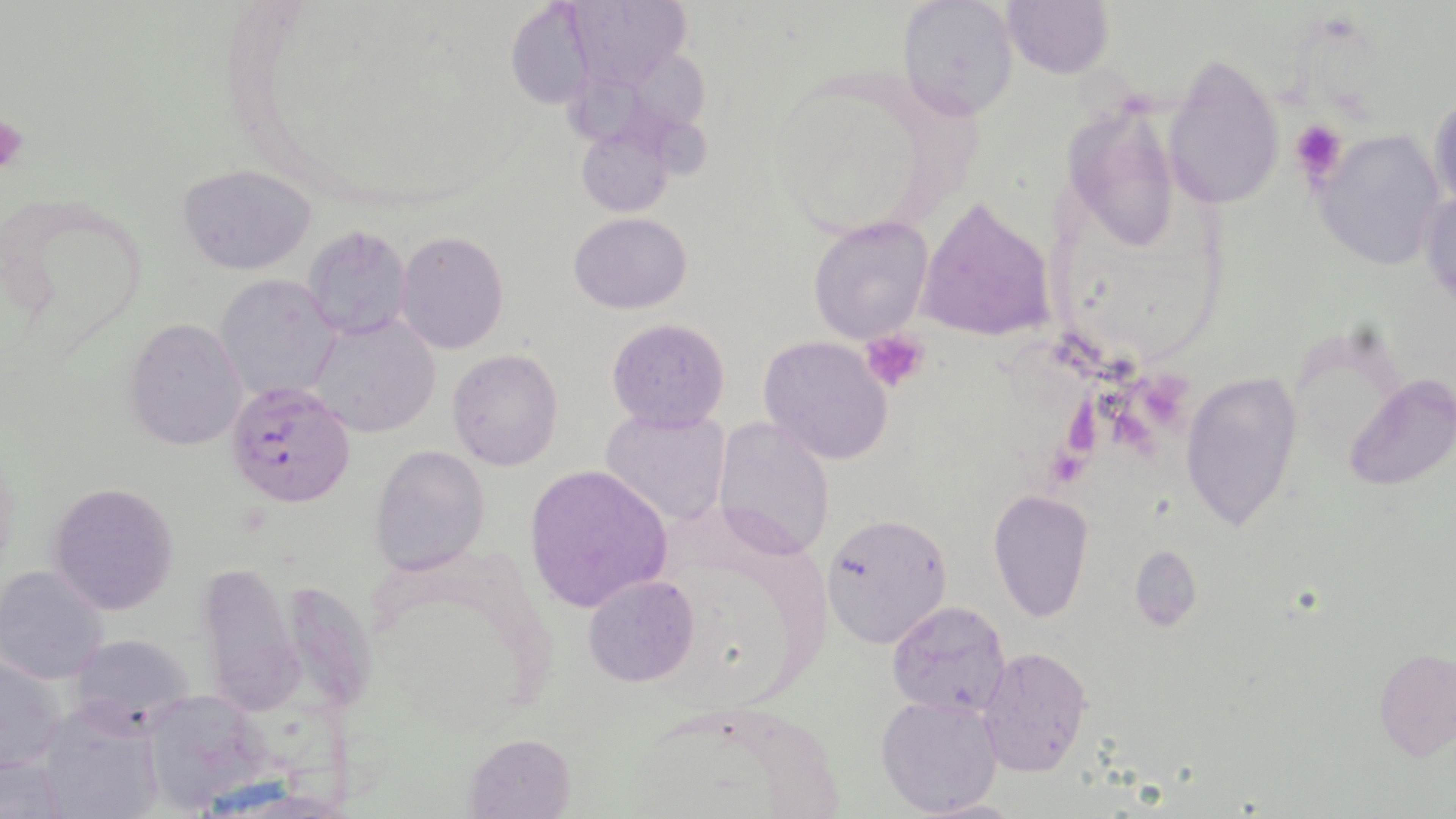

Summary:
  - Coordinate format: approximate bounding boxes as (x1,y1)-(x2,y2) corner pairs in pixels
  - Platelet locations: (0,112)-(28,177), (1289,117)-(1348,186), (860,330)-(932,394)
  - Uninfected red blood cell locations: (562,0)-(695,92), (1001,0)-(1115,78), (502,1)-(602,110), (896,1)-(1017,121), (1163,53)-(1284,211), (1429,89)-(1455,216), (1068,103)-(1178,259), (576,125)-(677,216), (1313,129)-(1446,270), (177,163)-(317,276), (1420,185)-(1455,311), (917,196)-(1058,344), (568,212)-(693,313), (806,215)-(933,345), (300,223)-(414,342), (395,232)-(509,354), (215,273)-(341,405), (310,315)-(441,438), (124,317)-(246,451), (606,317)-(732,434), (332,320)-(459,520), (758,335)-(895,465), (447,349)-(564,472), (1179,370)-(1305,534), (1343,375)-(1454,491), (598,406)-(733,529), (711,417)-(835,559), (369,444)-(490,575), (523,463)-(674,613), (47,480)-(181,616), (987,490)-(1094,623), (822,511)-(951,647), (1128,545)-(1201,632), (193,559)-(305,716), (1,564)-(112,685), (582,574)-(699,688), (296,583)-(383,706), (886,601)-(1014,717), (66,633)-(196,730), (976,646)-(1092,778), (1374,646)-(1455,763), (1,653)-(66,774), (147,689)-(265,795), (876,693)-(1004,818), (36,707)-(162,819), (464,732)-(579,819), (0,754)-(68,819), (920,797)-(1030,817)
  - Plasmodium falciparum-infected red blood cell locations: (225,377)-(357,509)
  - Slide-level diagnosis: Plasmodium falciparum
  - Field of view: single
  - Magnification: 1000x
  - Preparation: thin blood film
  - Image size: 1456×819 pixels
  - Modality: optical microscopy
  - Stain: May-Grünwald-Giemsa